Identify the parasite.
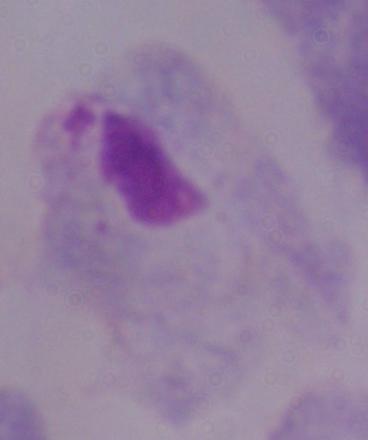

This is a trichomonad.

Captured at 1000x magnification. Micrograph.